Classify this cell by malaria status.
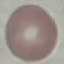
It is uninfected.

Summary:
  - Stain: Giemsa
  - Capture: smartphone camera at the microscope eyepiece
  - Image type: cell patch, automatically extracted from a larger field of view and resized to 64 × 64 pixels
  - Preparation: thin blood film